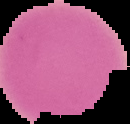

preparation = thin blood smear
image type = segmented cell region on a black background
image size = 130×124 pixels
result = Plasmodium parasites identified